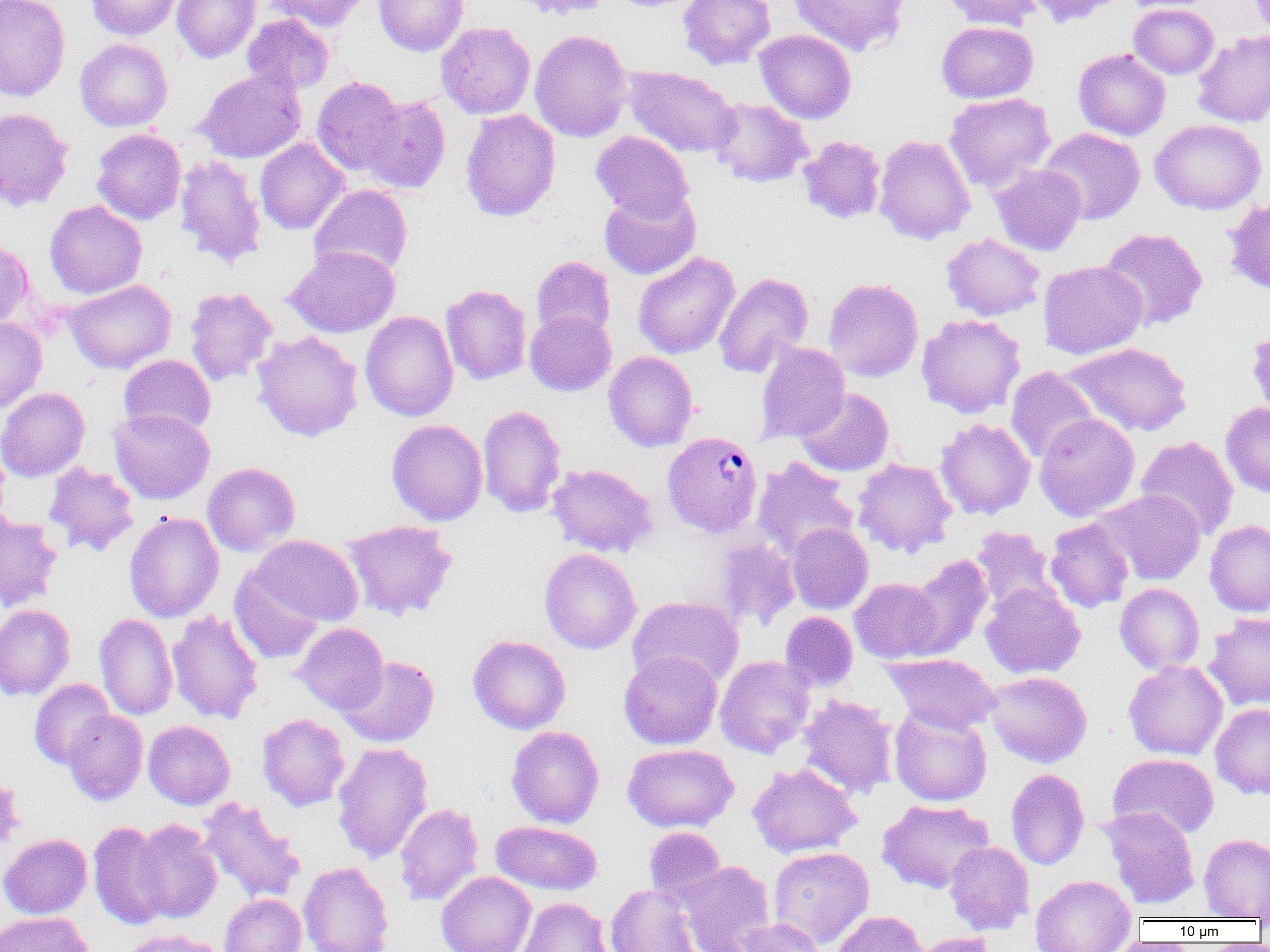

Approximate bounding boxes as [x1, y1, x2, y2] in pixels. Uninfected red blood cell locations: [0, 0, 71, 102], [85, 0, 182, 40], [172, 0, 260, 63], [264, 0, 371, 31], [374, 0, 469, 56], [509, 0, 614, 20], [678, 0, 776, 70], [789, 0, 910, 56], [941, 0, 1042, 30], [1022, 0, 1122, 27], [1129, 3, 1219, 79], [242, 15, 334, 95], [936, 21, 1038, 103], [436, 22, 536, 119], [529, 29, 632, 142], [754, 29, 857, 124], [1192, 31, 1270, 127], [75, 38, 172, 131], [1073, 49, 1171, 141], [622, 65, 741, 159], [196, 69, 306, 163], [312, 76, 406, 176], [944, 93, 1056, 193], [359, 95, 451, 193], [709, 98, 813, 188], [0, 107, 74, 211], [460, 109, 560, 222], [1150, 119, 1266, 215], [1037, 127, 1145, 225], [91, 128, 186, 225], [591, 131, 694, 223], [797, 135, 886, 225], [874, 135, 976, 244], [254, 138, 349, 235], [174, 154, 267, 269], [989, 164, 1086, 256], [309, 184, 412, 279], [599, 187, 701, 281], [1222, 196, 1270, 297], [44, 200, 147, 299], [1099, 228, 1208, 330], [941, 233, 1045, 321], [0, 238, 34, 330], [285, 246, 400, 337], [632, 251, 739, 359], [531, 256, 616, 340], [1038, 260, 1147, 359], [714, 272, 814, 378], [823, 278, 923, 382], [65, 279, 176, 374], [441, 284, 532, 385], [185, 287, 278, 386], [525, 310, 616, 396], [360, 311, 458, 422], [916, 314, 1026, 418], [0, 317, 47, 413], [251, 331, 363, 441], [755, 342, 850, 443], [1061, 342, 1192, 437], [603, 351, 698, 452], [119, 354, 216, 438], [1006, 367, 1100, 463], [0, 387, 90, 481], [795, 387, 894, 477], [1221, 402, 1270, 498], [478, 404, 567, 518], [108, 408, 215, 504], [1034, 413, 1140, 521], [934, 418, 1036, 519], [386, 419, 488, 526], [1135, 435, 1239, 539], [752, 457, 859, 560], [853, 457, 957, 558], [43, 461, 139, 557], [202, 462, 300, 556], [546, 464, 659, 558], [1094, 489, 1206, 586], [0, 511, 62, 611], [123, 512, 224, 622], [1045, 518, 1134, 613], [342, 519, 458, 621], [1204, 519, 1270, 617], [786, 523, 873, 614], [969, 525, 1062, 615], [249, 534, 363, 627], [713, 537, 799, 629], [539, 548, 641, 654], [903, 555, 993, 660], [229, 565, 326, 664], [849, 578, 945, 663], [980, 582, 1085, 679], [1115, 583, 1205, 675], [628, 596, 744, 688], [0, 604, 75, 700], [166, 609, 264, 725], [780, 611, 858, 692], [1204, 612, 1270, 711], [94, 613, 177, 720], [293, 623, 389, 715], [468, 634, 571, 734], [618, 651, 722, 749], [882, 653, 1001, 733], [714, 655, 815, 758], [337, 656, 439, 748], [1123, 659, 1228, 760], [983, 671, 1092, 767], [29, 678, 115, 769], [798, 694, 899, 799], [1210, 703, 1270, 800], [889, 706, 992, 806], [61, 709, 148, 805], [257, 713, 350, 811], [143, 720, 235, 809], [506, 725, 604, 828], [332, 742, 433, 864], [622, 743, 738, 832], [1108, 753, 1219, 839], [747, 762, 862, 858], [1006, 768, 1089, 869], [0, 771, 24, 858], [198, 796, 305, 904], [876, 799, 994, 893], [394, 803, 484, 906], [1099, 806, 1200, 909], [131, 819, 222, 924], [490, 820, 602, 895], [88, 821, 171, 929], [644, 826, 728, 907], [0, 833, 92, 918], [1199, 833, 1270, 920], [944, 841, 1034, 934], [768, 846, 874, 948], [678, 860, 777, 952], [298, 862, 394, 952], [436, 872, 536, 952], [1030, 874, 1137, 951], [605, 884, 701, 952], [220, 894, 306, 952], [516, 897, 614, 952], [830, 910, 929, 951], [0, 912, 95, 952], [732, 918, 825, 951], [122, 928, 227, 952], [910, 932, 999, 952]. Plasmodium vivax-infected red blood cell locations: [662, 431, 762, 537]. Slide-level diagnosis: Plasmodium vivax. Optical microscopy. Image is 1270×952 pixels. Thin blood smear. Captured at 1000x magnification. One field of a larger specimen.